Outline each blood parasite and name the species.
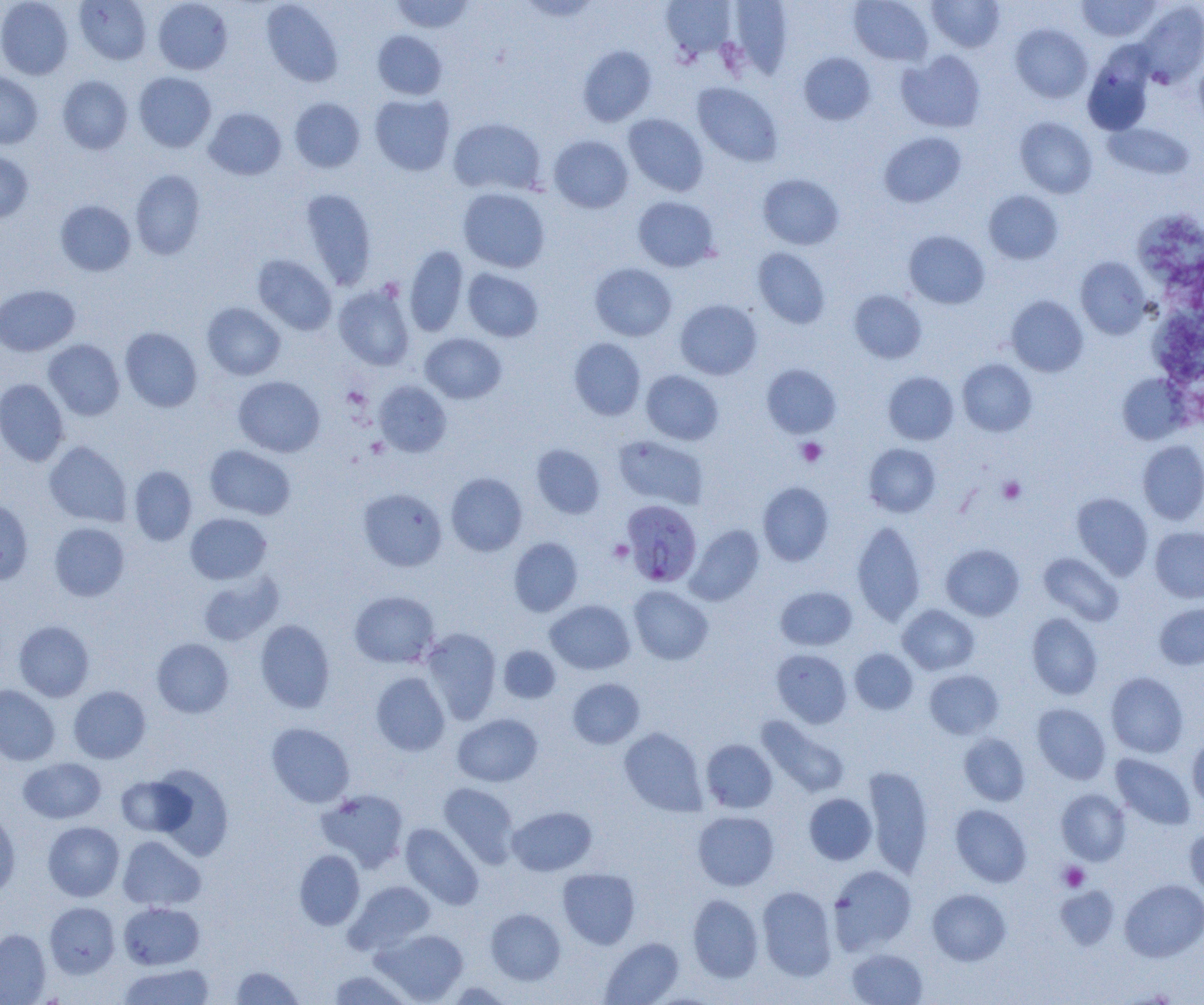

Approximate bounding boxes as (x1, y1, x2, y2) in pixels.
Plasmodium falciparum-infected red blood cells: (622, 509, 700, 587).
No Plasmodium ovale, Plasmodium malariae, Plasmodium vivax, Babesia divergens, or Trypanosoma brucei observed.

Platelet locations: (796, 438, 827, 467), (998, 476, 1026, 503), (609, 540, 633, 563), (1058, 862, 1089, 891). Uninfected red blood cell locations: (0, 0, 73, 80), (75, 0, 152, 65), (152, 0, 233, 75), (261, 0, 343, 87), (390, 0, 476, 33), (728, 0, 794, 77), (849, 0, 933, 66), (927, 0, 1005, 52), (661, 1, 738, 60), (1077, 1, 1161, 41), (1134, 2, 1204, 87), (1010, 24, 1092, 102), (372, 30, 447, 100), (577, 45, 657, 127), (897, 50, 985, 132), (799, 51, 875, 125), (1083, 51, 1154, 136), (1194, 53, 1204, 132), (0, 70, 42, 149), (133, 72, 216, 152), (57, 75, 132, 154), (692, 82, 783, 166), (370, 94, 455, 175), (289, 97, 365, 173), (204, 107, 287, 180), (623, 114, 708, 196), (448, 117, 546, 196), (1014, 117, 1097, 198), (1103, 122, 1194, 180), (879, 132, 966, 207), (548, 135, 633, 213), (0, 150, 33, 224), (130, 169, 206, 260), (758, 173, 844, 250), (300, 188, 377, 290), (458, 188, 550, 273), (983, 190, 1063, 264), (632, 196, 719, 272), (55, 199, 136, 276), (1135, 208, 1204, 289), (903, 230, 990, 309), (405, 245, 469, 337), (753, 247, 830, 328), (252, 254, 337, 335), (1075, 257, 1151, 339), (589, 263, 677, 341), (462, 268, 543, 342), (0, 284, 80, 357), (334, 284, 415, 371), (849, 290, 927, 363), (1006, 295, 1088, 377), (675, 299, 762, 379), (202, 302, 285, 380), (1140, 307, 1204, 384), (120, 327, 203, 412), (420, 333, 507, 404), (569, 338, 645, 420), (43, 339, 125, 420), (957, 359, 1037, 436), (762, 364, 841, 438), (641, 370, 723, 445), (883, 371, 959, 445), (1117, 374, 1189, 444), (233, 376, 325, 457), (0, 378, 69, 466), (374, 381, 451, 457), (612, 435, 709, 509), (1138, 440, 1204, 524), (44, 441, 131, 527), (863, 443, 940, 517), (204, 444, 296, 520), (531, 444, 605, 518), (129, 465, 197, 545), (445, 472, 528, 556), (757, 482, 834, 565), (358, 488, 447, 572), (1072, 493, 1152, 579), (0, 498, 33, 585), (185, 513, 271, 584), (851, 520, 926, 625), (49, 522, 130, 601), (686, 525, 764, 605), (1150, 527, 1204, 603), (509, 537, 583, 616), (941, 544, 1025, 621), (1038, 552, 1124, 625), (197, 571, 283, 646), (628, 585, 713, 665), (776, 586, 857, 650), (349, 590, 440, 668), (545, 599, 635, 674), (1155, 603, 1204, 670), (898, 604, 979, 675), (1026, 613, 1103, 700), (255, 619, 335, 713), (14, 620, 95, 701), (421, 628, 501, 723), (152, 637, 234, 718), (498, 645, 561, 704), (850, 648, 918, 715), (771, 649, 852, 728), (924, 669, 1003, 739), (1105, 671, 1188, 758), (370, 672, 450, 756), (567, 678, 644, 749), (0, 684, 60, 765), (69, 686, 150, 763), (1032, 703, 1111, 784), (453, 713, 542, 787), (757, 716, 850, 798), (266, 723, 355, 808), (619, 727, 707, 816), (959, 733, 1030, 805), (1187, 735, 1204, 810), (701, 739, 777, 813), (1110, 753, 1195, 829), (18, 757, 106, 824), (149, 764, 234, 860), (862, 766, 934, 877), (116, 776, 191, 837), (438, 783, 519, 867), (315, 788, 410, 873), (1056, 789, 1130, 865), (804, 793, 877, 865), (951, 804, 1031, 887), (507, 806, 597, 876), (0, 809, 21, 898), (692, 810, 779, 891), (43, 821, 124, 901), (400, 823, 484, 909), (1184, 824, 1204, 897), (118, 835, 205, 911), (294, 850, 365, 930), (828, 865, 916, 954), (557, 868, 640, 949), (1120, 879, 1204, 962), (345, 880, 436, 954), (757, 886, 837, 980), (1055, 886, 1119, 948), (927, 889, 1011, 966), (687, 893, 763, 982), (45, 902, 120, 978), (119, 902, 205, 970), (485, 908, 565, 985), (373, 928, 468, 1003), (0, 929, 51, 1004), (599, 937, 684, 1005), (846, 948, 928, 1005), (118, 963, 215, 1005), (230, 965, 304, 1004), (328, 969, 413, 1004), (443, 981, 514, 1005). Slide-level diagnosis: Plasmodium falciparum. Single field of view. Light microscopy. Thin blood smear. 1000x magnification. Image is 1204×1005 pixels.